Classify this cell by malaria status.
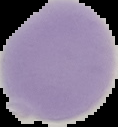
Uninfected.

preparation = thin blood smear
image size = 118×127 pixels
image type = cell region segmented out of the field of view; surrounding area masked to black